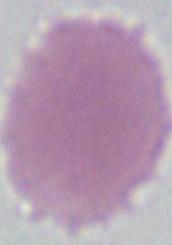
Summary:
  - Identification: red blood cell
  - Magnification: 1000x
  - Modality: photomicrograph